State which parasite is depicted.
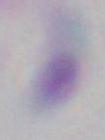
This is Toxoplasma gondii.

{
  "modality": "micrograph",
  "magnification": "1000x"
}